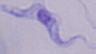
A trypanosome is shown. Captured at 1000x magnification. Micrograph.